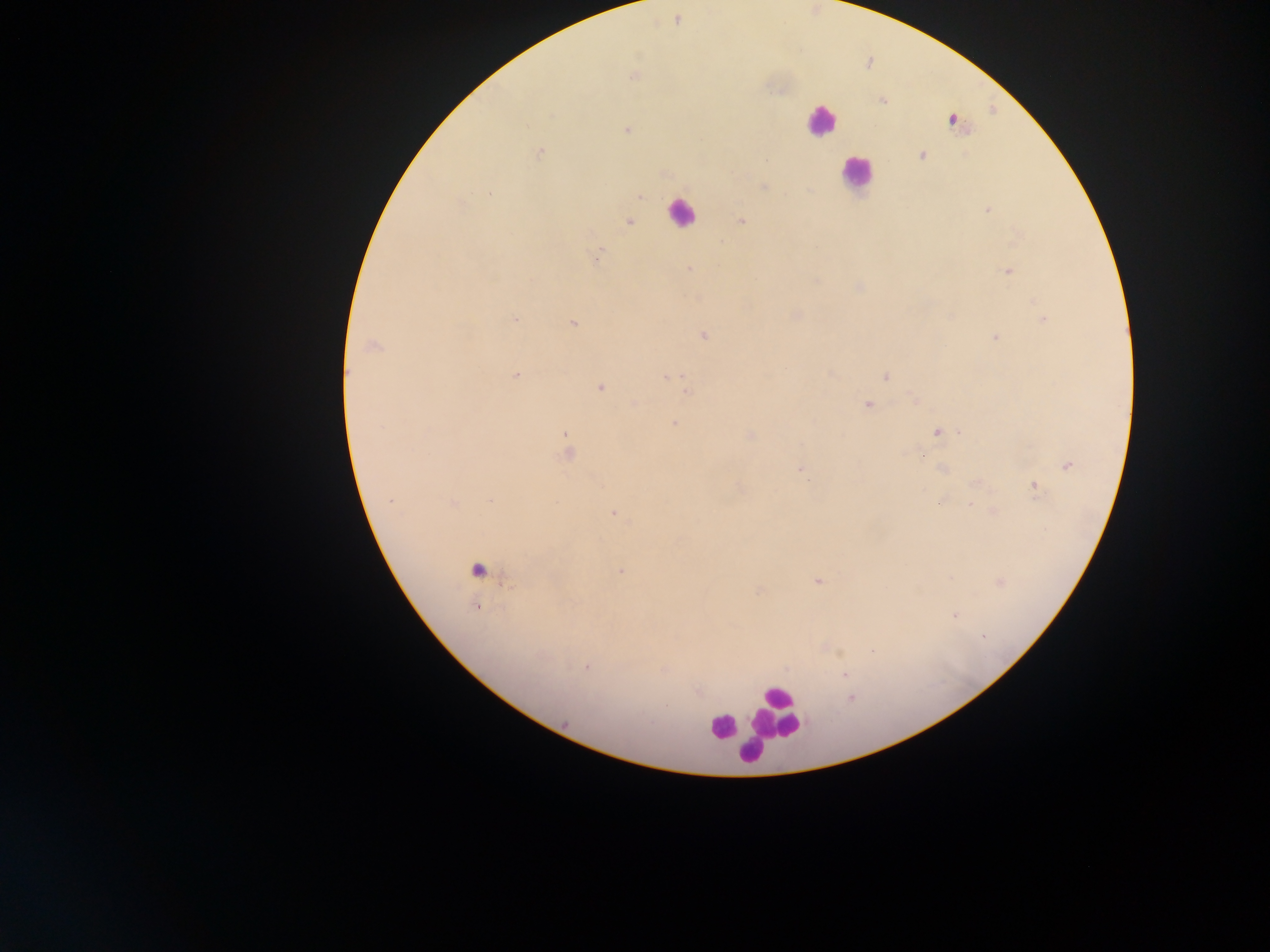
Approximate centers as {x, y} in pixels. Leukocyte locations: {821, 121}, {856, 173}, {680, 213}, {476, 570}, {776, 712}, {722, 726}, {749, 751}. Plasmodium parasite locations: {677, 20}, {634, 75}, {952, 121}, {627, 129}, {539, 153}, {922, 155}, {765, 160}, {765, 187}, {490, 193}, {640, 197}, {987, 209}, {741, 221}, {629, 222}, {597, 255}, {690, 268}, {1009, 272}, {859, 287}, {515, 319}, {1043, 319}, {573, 324}, {703, 335}, {994, 338}, {372, 346}, {517, 375}, {884, 377}, {667, 378}, {600, 387}, {686, 391}, {867, 405}, {675, 423}, {937, 432}, {960, 432}, {567, 434}, {749, 435}, {566, 454}, {1068, 465}, {800, 469}, {942, 469}, {975, 484}, {1034, 486}, {391, 500}, {490, 500}, {453, 503}, {971, 506}, {613, 514}, {621, 571}, {818, 581}, {476, 607}, {954, 616}, {983, 636}, {872, 651}, {587, 667}, {844, 675}, {851, 699}, {565, 723}. Mobile-phone photograph taken through the microscope. Single field of view. Thick blood smear. Sample from Ghana. Image is 1270×952 pixels.